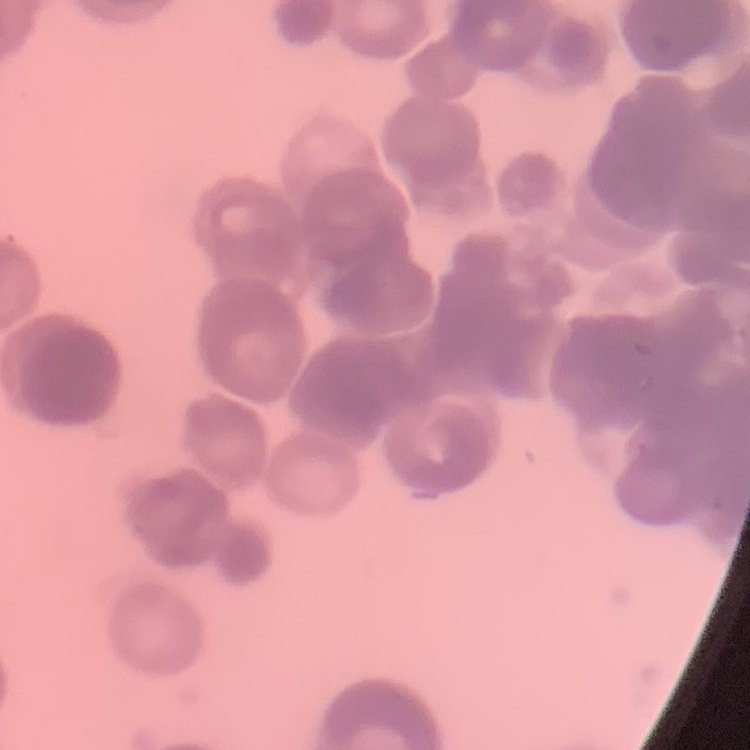
erythrocyte morphology = rouleaux formation
preparation = thin peripheral smear
image type = one tile cut from a larger photomicrograph
stain = Field's or Giemsa